Locate Plasmodium parasites and leukocytes.
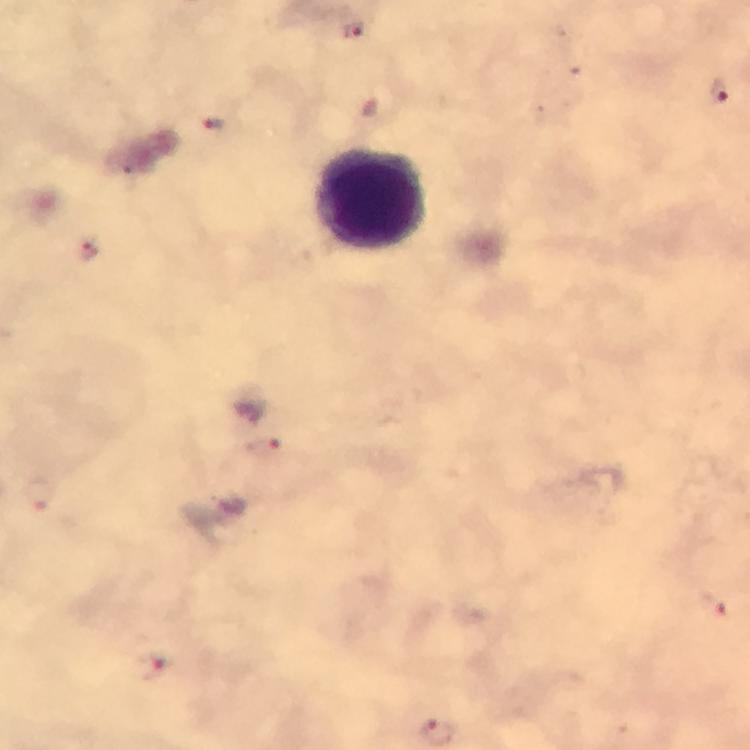
Approximate centers as [x, y] in pixels.
Plasmodium parasites: [356, 32], [719, 92], [215, 123], [89, 250], [264, 449], [716, 603], [153, 667].
Leukocytes: [371, 201].

From a diagnostic examination for malaria. 100x magnification. Thick smear. Immersion oil applied. Image is 750×750 pixels. A crop from one field of view. Giemsa stain. Photographed with a smartphone mounted on the microscope.